Assess this cell for malaria.
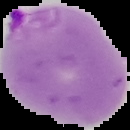
Parasitized.

From a thin blood smear. Image is 130×130 pixels. The area outside the segmented cell region is set to black.